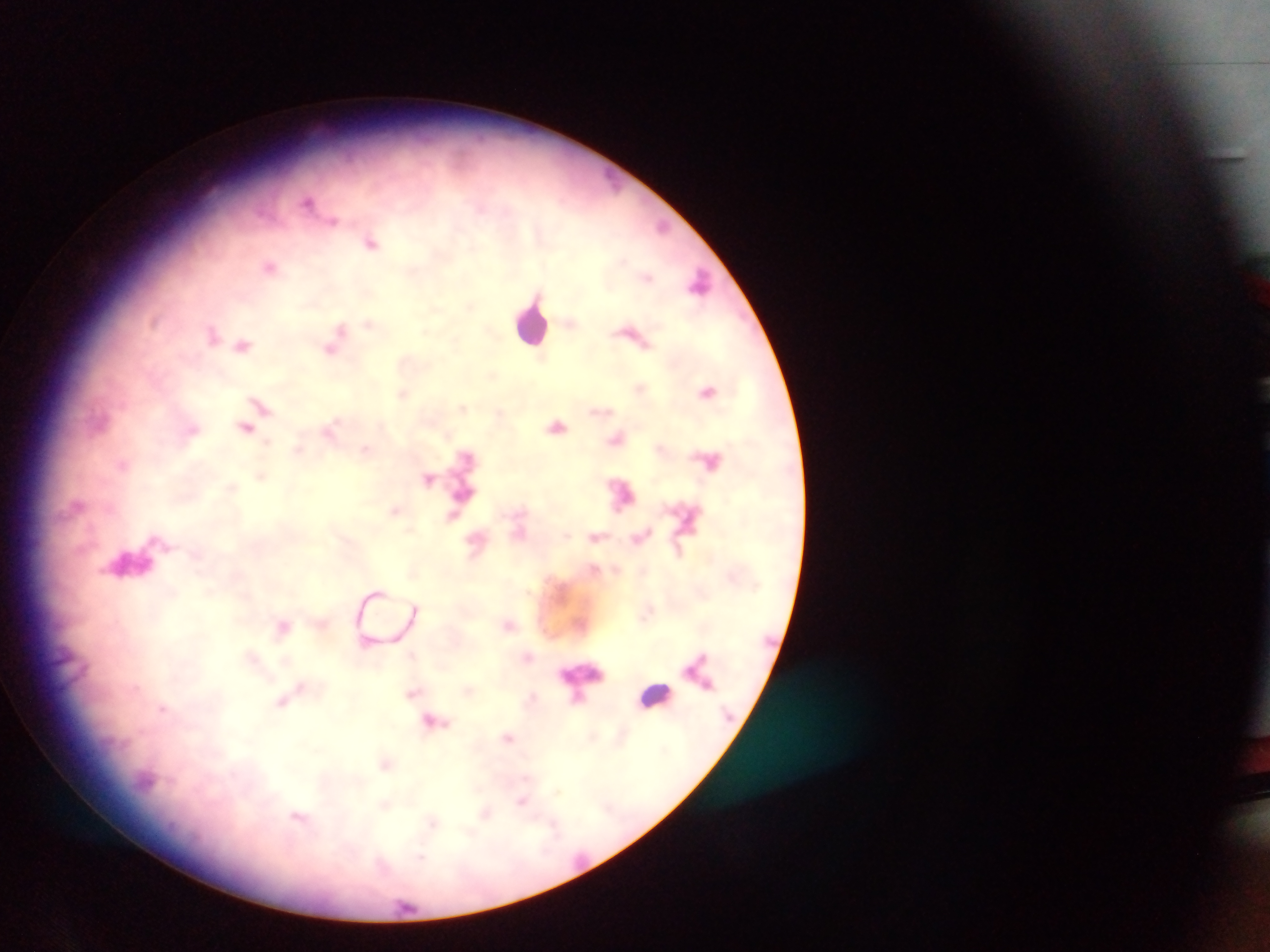
Approximate centers as [x, y] in pixels. Malaria parasite locations: [309, 201], [333, 221], [662, 226], [371, 242], [270, 266], [648, 277], [699, 281], [470, 306], [368, 323], [340, 328], [212, 334], [243, 345], [331, 349], [707, 391], [403, 393], [261, 406], [461, 408], [557, 425], [244, 427], [193, 430], [330, 430], [616, 439], [298, 448], [365, 449], [121, 464], [261, 475], [428, 480], [231, 487], [394, 510], [452, 516], [595, 537], [415, 607], [508, 625], [282, 626], [412, 654], [252, 657], [700, 657], [298, 689], [468, 690], [412, 693], [532, 697], [283, 701], [162, 708], [432, 722], [508, 737], [386, 764], [556, 791], [522, 802], [386, 805], [485, 813], [298, 818], [433, 823], [421, 857]. Leukocyte locations: [532, 323], [129, 565], [583, 676], [654, 695], [145, 783]. Image is 1270×952 pixels. Thick blood film. One field of view. Photographed through a microscope with a mobile-phone camera. Collected in Ghana.